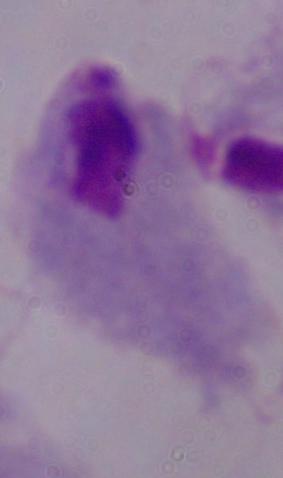
modality = photomicrograph
magnification = 1000x
identification = trichomonad